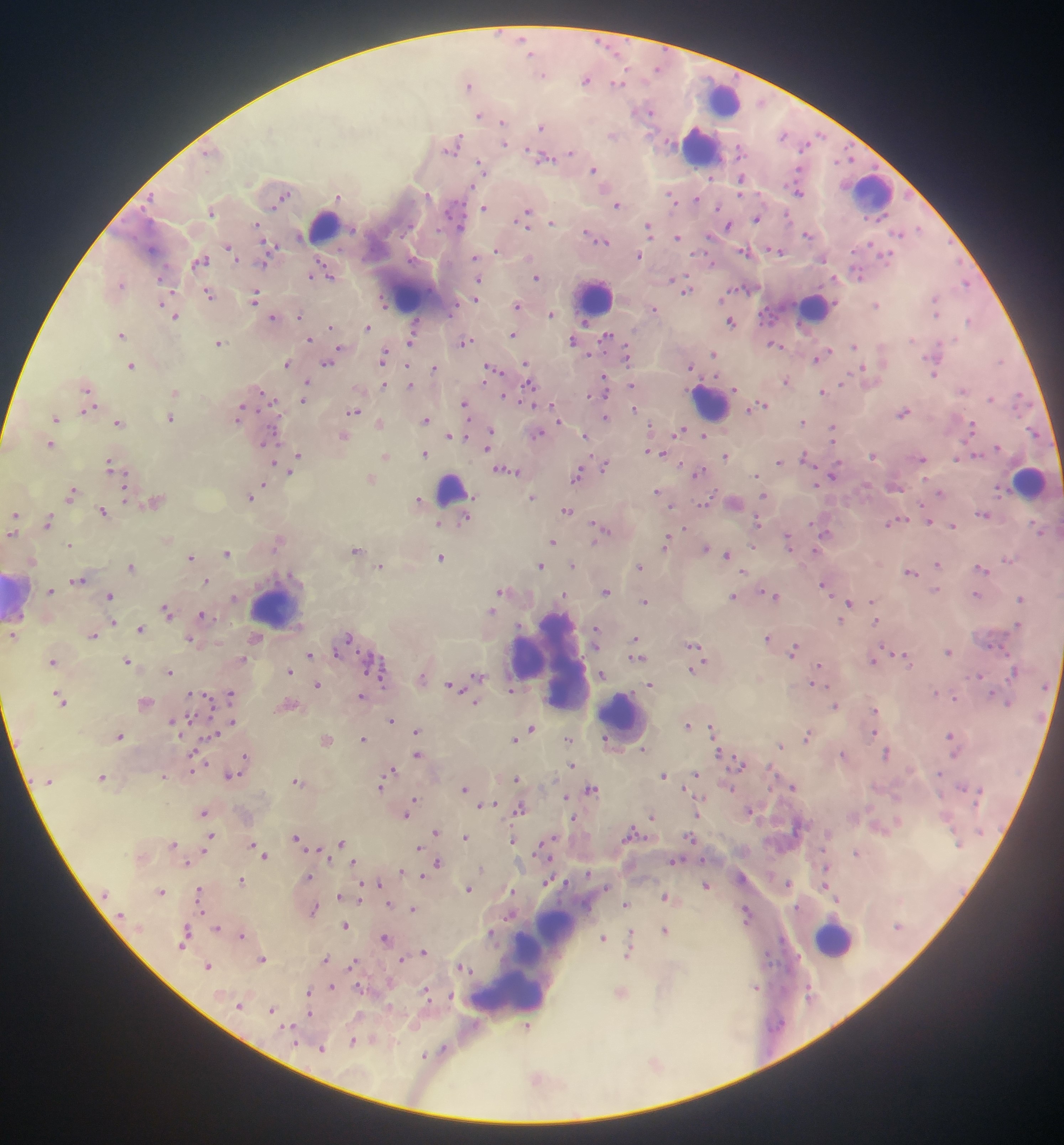
Approximate centers as x y in pixels. Malaria parasite locations: 530 53; 657 67; 542 73; 586 79; 617 83; 468 84; 646 111; 480 114; 503 123; 541 126; 613 135; 784 136; 667 142; 503 143; 452 144; 570 153; 542 157; 848 157; 481 167; 593 168; 741 179; 798 191; 281 196; 337 196; 670 197; 696 199; 617 203; 484 207; 718 207; 211 211; 525 215; 756 218; 552 222; 257 225; 727 225; 648 228; 916 228; 807 233; 709 236; 677 237; 596 238; 270 245; 229 248; 775 249; 496 250; 746 251; 639 256; 474 258; 200 260; 710 261; 264 262; 325 271; 858 273; 314 275; 536 276; 478 278; 834 278; 672 279; 118 283; 965 284; 686 289; 209 293; 254 298; 722 298; 167 299; 475 299; 936 301; 383 302; 517 304; 876 304; 169 309; 653 309; 551 313; 174 315; 299 315; 272 317; 731 321; 969 321; 415 324; 330 326; 367 327; 120 334; 513 334; 411 335; 606 336; 309 339; 411 341; 573 341; 464 342; 218 343; 774 343; 854 345; 339 349; 712 353; 626 354; 383 356; 819 356; 1000 360; 327 362; 286 363; 526 363; 131 365; 690 366; 434 368; 493 369; 863 370; 934 373; 604 380; 786 381; 306 383; 383 384; 410 385; 631 385; 529 386; 735 388; 963 389; 87 390; 305 390; 174 391; 823 391; 263 393; 1019 396; 303 398; 990 398; 465 403; 760 405; 634 408; 88 409; 353 411; 903 412; 239 413; 557 416; 55 417; 604 417; 170 418; 426 419; 802 421; 118 422; 379 422; 972 426; 832 428; 681 430; 449 434; 537 434; 703 434; 463 435; 490 435; 343 436; 585 436; 268 440; 50 444; 487 447; 997 447; 649 451; 425 453; 661 454; 385 455; 873 455; 298 456; 725 456; 805 457; 922 458; 957 458; 779 461; 273 463; 604 465; 110 466; 292 470; 507 471; 698 473; 577 475; 756 475; 832 475; 370 478; 264 484; 71 491; 656 491; 940 493; 764 496; 250 497; 532 497; 418 499; 155 500; 734 501; 566 510; 103 511; 984 514; 14 515; 466 517; 757 521; 896 521; 929 521; 47 522; 438 523; 952 526; 600 527; 684 528; 824 531; 1040 531; 11 532; 278 540; 552 540; 666 540; 788 540; 69 545; 752 546; 705 547; 356 549; 815 551; 226 553; 727 555; 190 556; 441 557; 1007 559; 32 560; 937 564; 540 565; 573 565; 131 566; 380 566; 639 566; 981 568; 910 571; 78 579; 206 581; 824 584; 504 589; 935 589; 50 590; 605 590; 773 594; 976 594; 109 595; 564 595; 733 596; 1021 597; 644 601; 848 603; 167 609; 491 611; 202 614; 875 620; 842 621; 112 622; 1017 625; 140 628; 596 630; 92 633; 11 635; 347 637; 767 638; 191 639; 255 639; 635 640; 636 648; 695 649; 793 650; 948 651; 337 654; 310 655; 897 655; 636 657; 904 657; 242 658; 872 660; 52 661; 127 662; 697 663; 820 666; 695 668; 289 670; 1014 670; 169 672; 478 675; 601 675; 978 675; 381 677; 422 678; 316 684; 649 684; 813 684; 454 685; 511 688; 936 692; 230 693; 992 693; 192 694; 59 696; 361 697; 954 697; 144 702; 474 702; 288 704; 834 705; 214 708; 875 710; 391 719; 172 721; 232 721; 687 724; 530 728; 711 729; 416 730; 874 732; 119 734; 212 734; 807 735; 951 736; 363 738; 569 739; 326 740; 514 740; 781 745; 195 747; 643 749; 719 752; 886 753; 843 754; 245 755; 418 755; 737 762; 571 765; 192 766; 391 770; 231 774; 663 774; 694 774; 163 775; 101 776; 516 778; 48 782; 297 782; 793 785; 381 786; 464 787; 590 789; 566 796; 414 798; 485 804; 519 808; 749 809; 203 811; 406 814; 697 814; 652 816; 573 818; 436 831; 210 836; 465 836; 296 837; 691 837; 512 840; 341 842; 172 845; 253 845; 543 847; 318 848; 418 848; 203 851; 856 853; 264 855; 675 859; 353 861; 186 863; 437 863; 480 868; 401 869; 825 869; 421 875; 308 876; 241 880; 548 881; 377 883; 788 883; 361 884; 705 884; 469 888; 160 891; 512 892; 198 893; 107 895; 339 896; 665 896; 834 898; 625 903; 388 904; 314 908; 412 908; 746 912; 509 915; 345 925; 216 927; 665 930; 185 932; 491 933; 631 934; 241 935; 385 938; 603 938; 182 943; 423 951; 628 952; 262 959; 325 959; 401 959; 353 963; 207 965; 462 966; 755 986; 331 987; 309 991; 426 992; 620 992; 450 995; 240 1005; 272 1009; 309 1014; 290 1027; 527 1027; 353 1041; 321 1048; 442 1050; 424 1055; 654 1062; 536 1079. Leukocyte locations: 722 100; 701 145; 870 193; 323 224; 410 290; 593 298; 814 307; 709 401; 1028 480; 451 489; 18 597; 275 604; 553 660; 623 717; 556 925; 833 938; 509 987. Sample from Ghana. Thick blood smear. Image is 1064×1145 pixels. Mobile-phone photograph taken through the microscope. Single field of view.